Assess the morphology of the red blood cells.
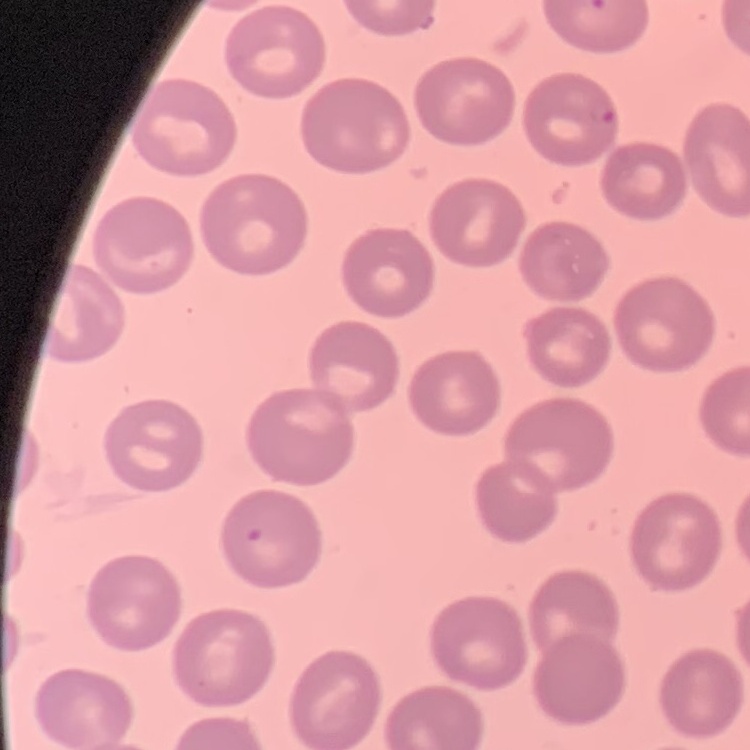

They show no rouleaux formation.

Summary:
  - Stain: Field's or Giemsa
  - Preparation: thin peripheral smear
  - Image type: square crop of a larger photomicrograph